Assess the morphology of the red blood cells.
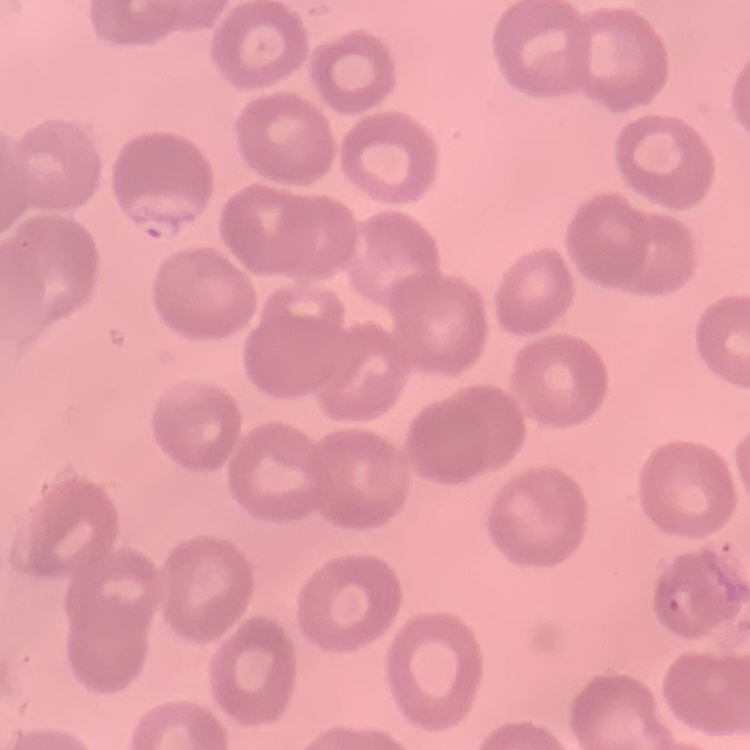

They show no rouleaux formation.

image type = one tile cut from a larger photomicrograph
stain = Field's or Giemsa
preparation = thin blood smear